Locate every blood parasite and identify its species.
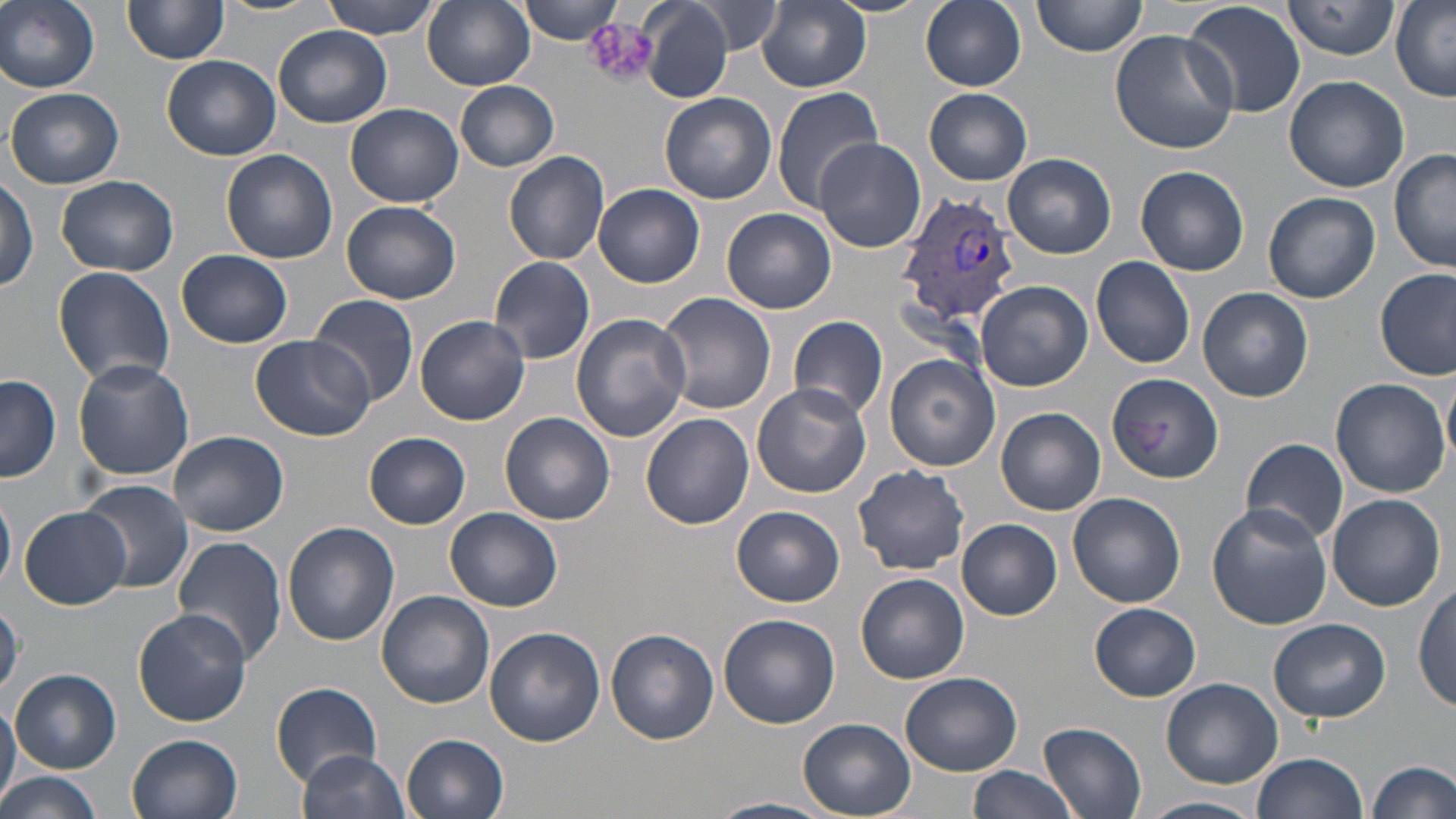

Approximate bounding boxes as (x1,y1)-(x2,y2) corner pairs in pixels.
Plasmodium vivax-infected red blood cells: (894,189)-(1023,324).
No Plasmodium falciparum, Plasmodium ovale, Plasmodium malariae, Babesia divergens, or Trypanosoma brucei observed.

Summary:
  - Uninfected red blood cell locations: (0,0)-(100,92), (214,0)-(319,16), (321,0)-(441,39), (423,0)-(535,91), (517,0)-(626,43), (758,0)-(871,91), (919,0)-(1027,91), (1033,0)-(1147,57), (1183,0)-(1307,118), (1283,0)-(1400,59), (1391,0)-(1456,103), (637,1)-(734,103), (122,2)-(227,66), (696,2)-(782,55), (273,25)-(392,128), (1109,29)-(1239,154), (162,55)-(281,162), (1284,74)-(1409,192), (453,79)-(560,171), (770,86)-(882,212), (5,87)-(125,188), (924,89)-(1032,185), (660,93)-(777,204), (345,103)-(465,206), (814,137)-(926,253), (1389,148)-(1455,273), (221,149)-(338,264), (503,151)-(611,266), (1004,153)-(1116,259), (1135,165)-(1250,276), (55,173)-(180,275), (0,176)-(38,295), (594,184)-(705,287), (1264,192)-(1380,304), (342,201)-(461,306), (721,208)-(836,314), (176,250)-(294,349), (489,256)-(596,365), (1091,256)-(1194,368), (53,267)-(176,389), (1375,267)-(1455,380), (977,281)-(1092,391), (1199,288)-(1314,402), (656,291)-(776,415), (308,293)-(420,406), (572,313)-(691,442), (414,314)-(529,424), (788,316)-(888,422), (251,333)-(374,441), (885,354)-(999,471), (73,358)-(194,481), (1443,369)-(1456,470), (1107,372)-(1224,483), (1,375)-(61,483), (1329,377)-(1449,497), (752,382)-(871,497), (997,406)-(1105,515), (501,412)-(615,526), (641,413)-(754,529), (168,431)-(289,535), (365,433)-(471,530), (1241,438)-(1349,545), (851,465)-(971,575), (79,479)-(193,595), (0,489)-(15,592), (1066,492)-(1186,608), (1326,494)-(1446,611), (1206,504)-(1332,630), (19,506)-(130,608), (732,506)-(845,606), (445,507)-(562,611), (958,519)-(1062,619), (282,522)-(399,647), (170,536)-(288,666), (855,572)-(969,686), (1414,585)-(1455,711), (377,591)-(496,710), (1090,603)-(1201,701), (132,607)-(252,726), (717,611)-(838,730), (1269,617)-(1392,722), (485,627)-(605,748), (606,630)-(719,745), (10,669)-(121,773), (901,672)-(1022,776), (1160,678)-(1284,788), (272,682)-(382,784), (0,698)-(20,810), (799,718)-(918,819), (1039,722)-(1146,819), (127,733)-(243,819), (402,733)-(509,818), (298,748)-(412,819), (1250,752)-(1369,819), (1368,758)-(1455,819), (966,765)-(1084,819), (0,770)-(104,819), (711,796)-(833,819), (1144,796)-(1262,819)
  - Platelet locations: (585,21)-(659,87)
  - Slide-level diagnosis: Plasmodium vivax
  - Modality: optical microscopy
  - Preparation: thin blood film
  - Image size: 1456×819 pixels
  - Stain: May-Grünwald-Giemsa
  - Field of view: single
  - Magnification: 1000x